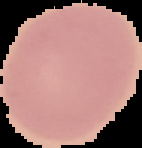

The area outside the segmented cell region is set to black. Image is 142×148 pixels. From a thin blood film. Malaria status: uninfected.